Classify this cell by malaria status.
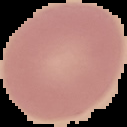

Uninfected.

preparation = thin blood smear
image size = 127×127 pixels
image type = segmented cell region with the area outside set to black